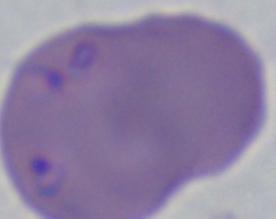 Micrograph. A Babesia parasite is shown. Captured at 1000x magnification.